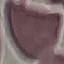
result = no malaria parasites seen
stain = Giemsa
preparation = thin blood smear
capture = smartphone camera at the microscope eyepiece
image type = automatically extracted cell patch, resized to 64 × 64 pixels